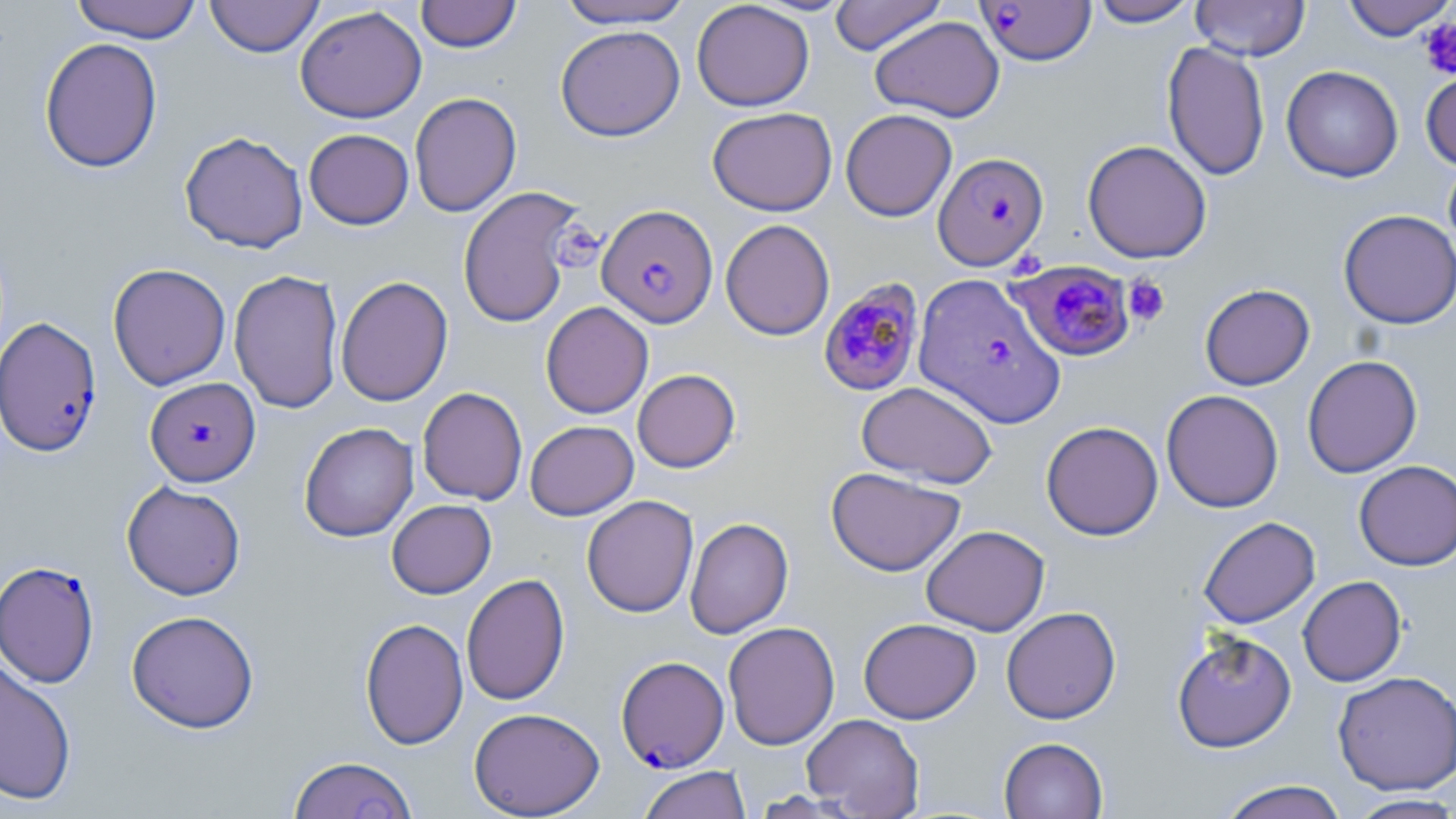
Summary:
  - Coordinate format: approximate bounding boxes as (x1,y1)-(x2,y2) corner pairs in pixels
  - Platelet locations: (1419,17)-(1456,80), (552,221)-(603,271), (1123,276)-(1171,327)
  - Plasmodium falciparum-infected red blood cell locations: (977,1)-(1096,66), (933,152)-(1049,271), (598,204)-(719,328), (1008,262)-(1137,363), (914,273)-(1067,430), (818,278)-(925,396), (0,316)-(103,456), (145,377)-(260,486), (0,560)-(100,688), (616,655)-(729,772)
  - Uninfected red blood cell locations: (70,0)-(203,43), (205,0)-(324,57), (415,0)-(522,53), (556,0)-(694,29), (829,0)-(946,55), (1089,0)-(1200,27), (1191,0)-(1310,60), (1341,0)-(1455,41), (691,1)-(814,111), (295,5)-(427,123), (870,16)-(1005,122), (555,24)-(685,141), (39,37)-(163,173), (1162,41)-(1270,181), (1281,65)-(1403,183), (1420,65)-(1456,171), (409,92)-(521,217), (706,107)-(838,216), (841,109)-(957,222), (304,128)-(414,229), (180,131)-(308,253), (1082,139)-(1212,264), (1443,157)-(1456,268), (457,186)-(584,328), (1338,209)-(1456,329), (720,219)-(835,340), (107,263)-(231,390), (229,269)-(344,413), (335,275)-(453,407), (1199,283)-(1315,390), (540,301)-(654,418), (1302,354)-(1422,478), (632,368)-(741,473), (857,381)-(997,488), (417,387)-(528,505), (1161,389)-(1284,513), (524,420)-(639,520), (1040,421)-(1164,540), (299,422)-(418,541), (1353,460)-(1456,571), (826,466)-(965,576), (121,480)-(246,600), (581,495)-(699,617), (386,499)-(496,598), (1198,516)-(1320,628), (684,517)-(793,639), (921,525)-(1050,636), (461,573)-(570,706), (1297,575)-(1407,687), (1000,606)-(1121,724), (126,609)-(259,733), (360,617)-(468,750), (858,618)-(981,724), (722,621)-(840,750), (1172,631)-(1297,752), (0,659)-(77,806), (1332,670)-(1456,795), (468,707)-(605,818), (801,713)-(925,817), (999,736)-(1108,819), (287,755)-(418,819), (637,766)-(751,819), (1217,780)-(1348,819), (1346,794)-(1456,818)
  - Slide-level diagnosis: Plasmodium falciparum
  - Field of view: one of a larger specimen
  - Image size: 1456×819 pixels
  - Stain: May-Grünwald-Giemsa
  - Magnification: 1000x
  - Modality: light microscopy
  - Preparation: thin blood film